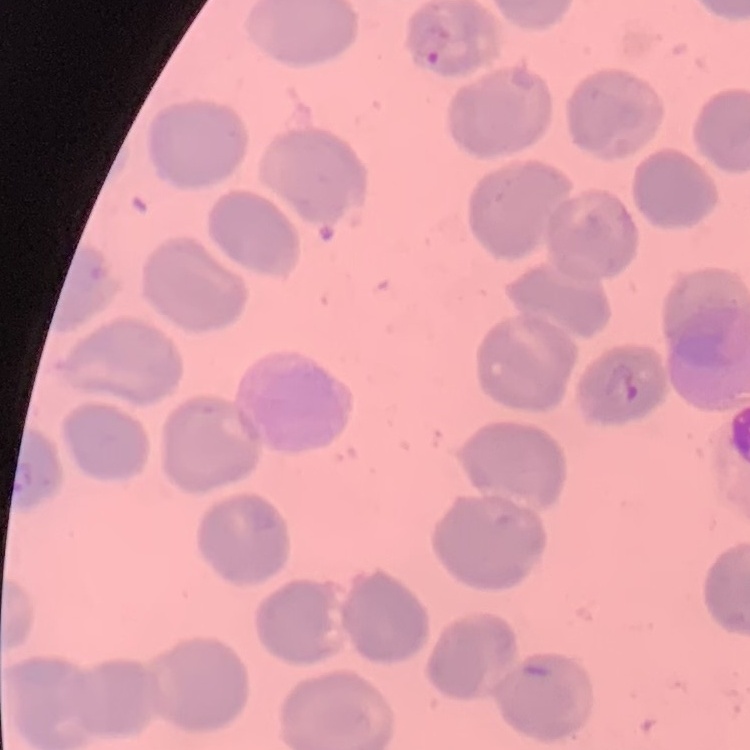
red blood cell morphology = no rouleaux formation
image type = one tile cut from a larger photomicrograph
preparation = thin peripheral smear
stain = Field's or Giemsa